Report the malaria status of this cell.
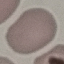
Uninfected.

Summary:
  - Stain: Giemsa
  - Image type: automatically extracted cell patch, resized to 64 × 64 pixels
  - Capture: smartphone through the microscope eyepiece
  - Preparation: thin blood film